State which parasite is depicted.
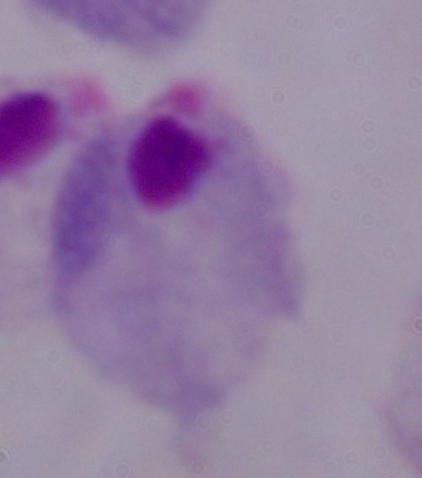

A trichomonad.

modality = photomicrograph
magnification = 1000x